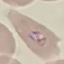

Malaria status: parasitized. Automatically extracted cell patch, resized to 64 × 64 pixels. Giemsa stain. Acquired by smartphone through the microscope eyepiece. Thin blood smear.